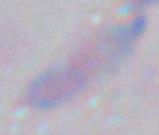 Toxoplasma gondii is shown. Micrograph. Captured at 1000x magnification.